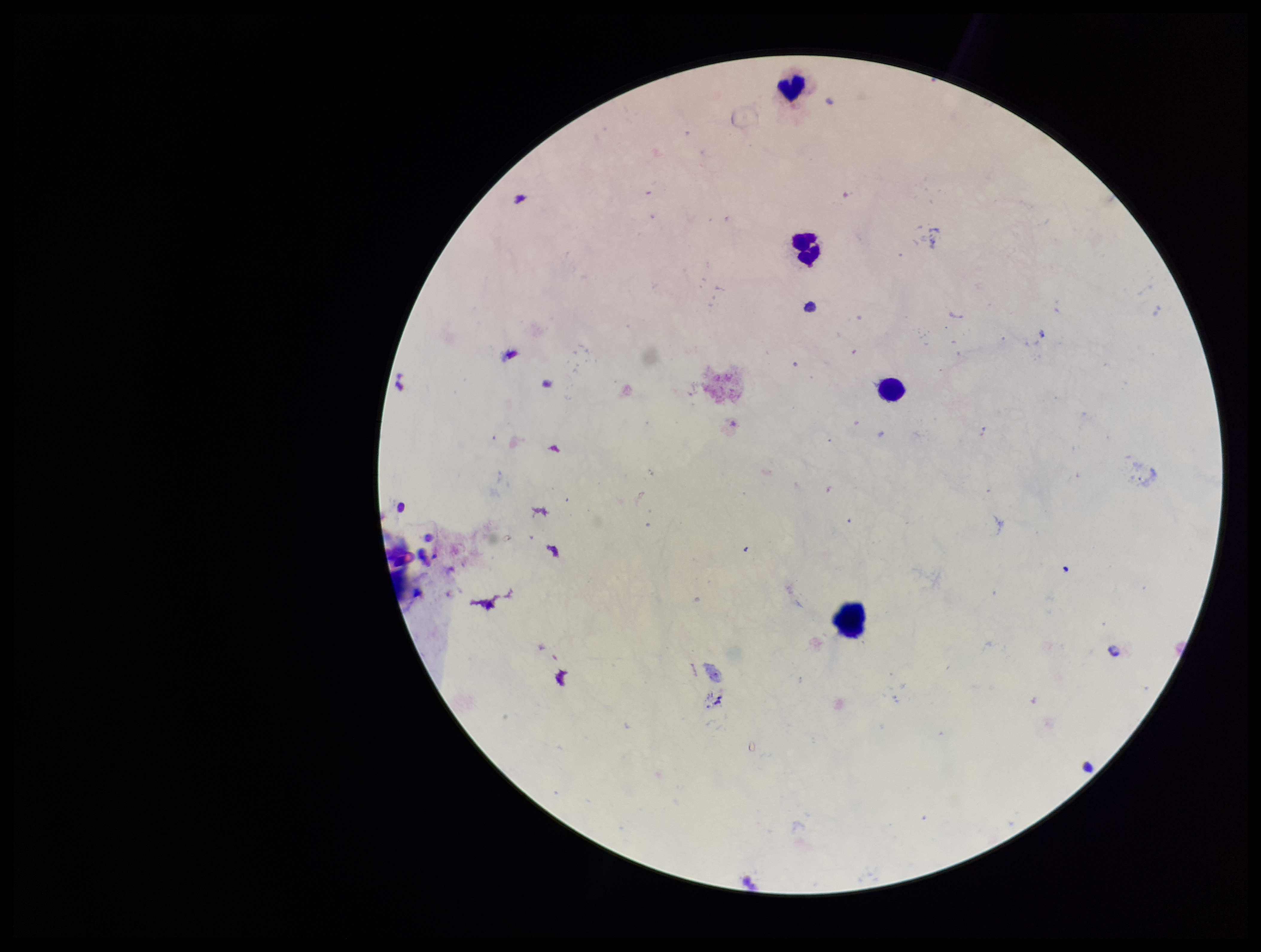
Summary:
  - Plasmodium parasites: none detected
  - Parasite count: 0
  - Image size: 1261×952 pixels
  - Capture: smartphone photograph through the microscope eyepiece
  - Leukocyte count: 4
  - Patient malaria status: negative
  - Preparation: thick blood smear
  - Stain: Giemsa
  - Field of view: single